Classify this cell by malaria status.
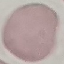

Uninfected.

preparation: thin blood smear
capture: smartphone through the microscope eyepiece
stain: Giemsa
image_type: automatically extracted cell patch, resized to 64 × 64 pixels